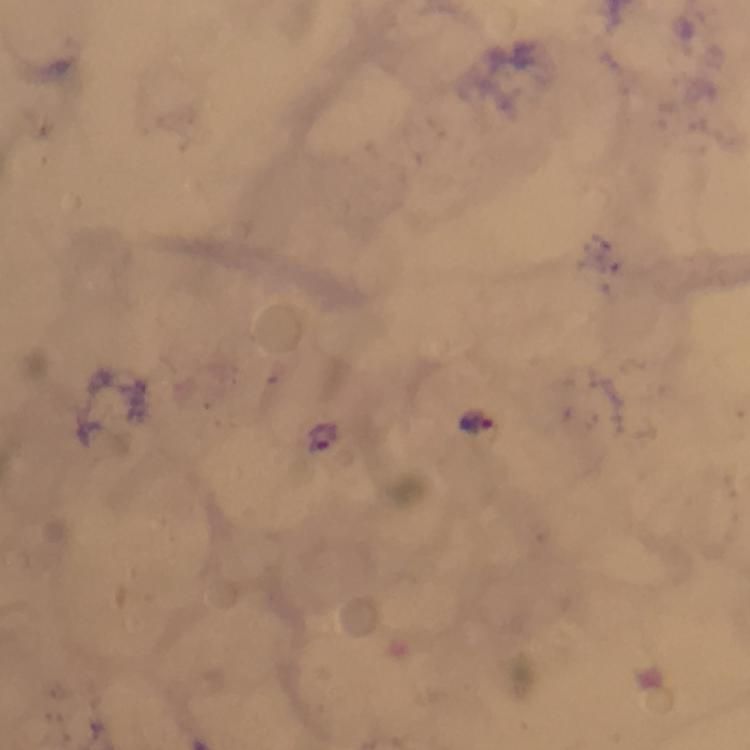
Approximate object centers, in pixels from the top-left corner.
Summary:
  - Plasmodium parasite locations: (x=477, y=422), (x=326, y=437)
  - Magnification: 100x
  - Cropped from: one field of view
  - Stain: Giemsa
  - Image size: 750×750 pixels
  - Context: from a malaria diagnostic workup
  - Preparation: thick smear
  - Capture: smartphone camera through the microscope
  - Immersion oil: applied